State which parasite is depicted.
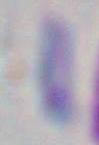
This is Toxoplasma gondii.

magnification = 1000x
modality = micrograph